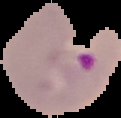

From a thin blood film. Image is 121×118 pixels. The area outside the segmented cell region is set to black. Result: Plasmodium parasites identified.